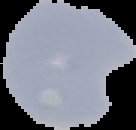
Cell region segmented out of the field of view; the surrounding area is masked to black. Image is 136×130 pixels. Malaria status: parasitized. From a thin blood smear.